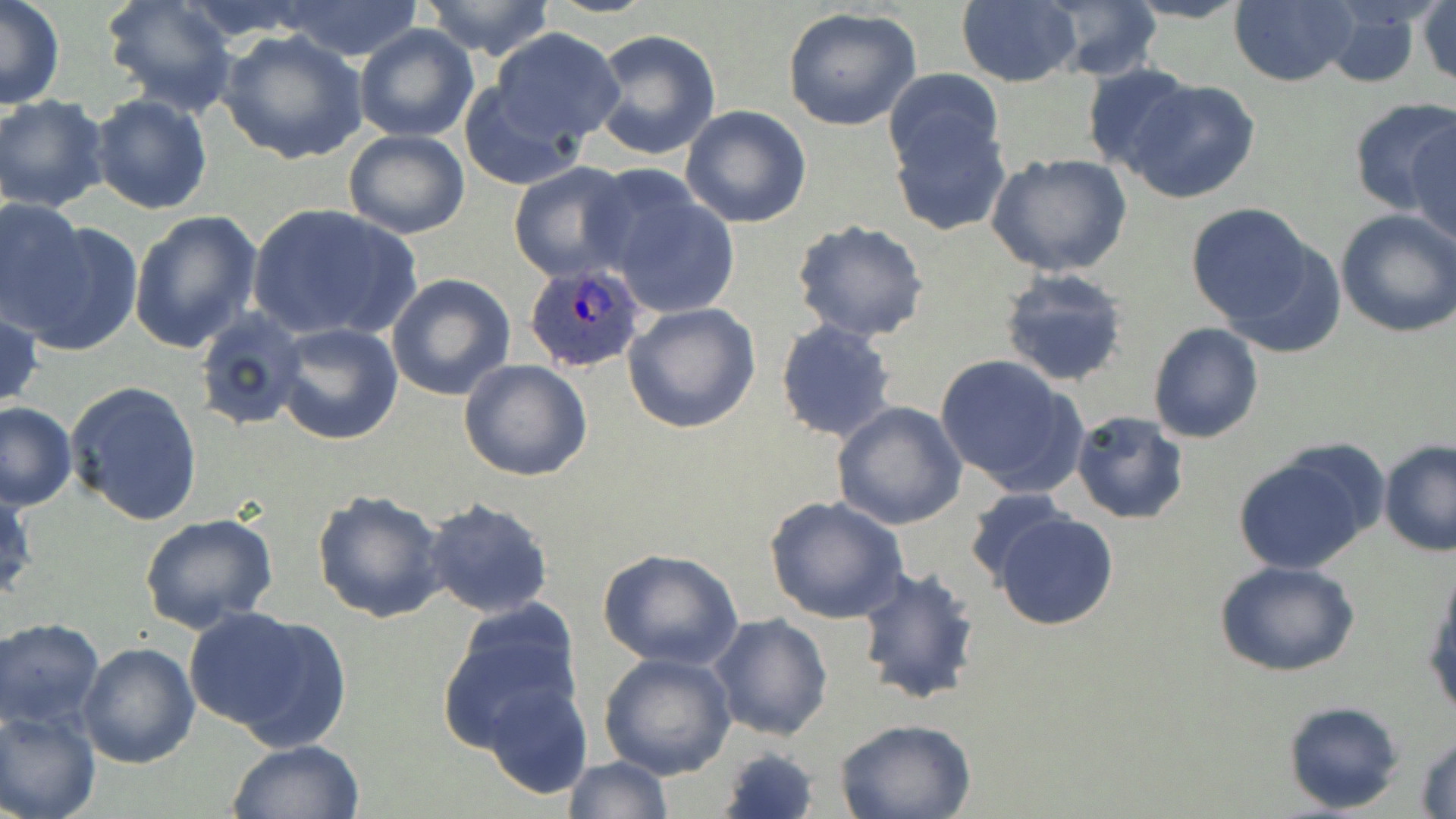
Summary:
  - Coordinate format: approximate bounding boxes as (x1,y1)-(x2,y2) corner pairs in pixels
  - Uninfected red blood cell locations: (0,0)-(66,110), (100,0)-(237,115), (419,0)-(558,60), (538,0)-(659,19), (956,0)-(1081,87), (1041,0)-(1162,81), (1119,0)-(1256,24), (1228,1)-(1357,87), (1418,1)-(1455,89), (277,3)-(426,61), (1320,5)-(1426,88), (782,6)-(923,133), (354,22)-(480,143), (489,28)-(627,147), (589,28)-(722,161), (216,29)-(369,165), (1081,63)-(1196,176), (883,67)-(1005,175), (1123,80)-(1262,204), (458,81)-(583,190), (89,92)-(214,215), (0,95)-(109,212), (1348,95)-(1454,219), (681,104)-(812,228), (889,110)-(1011,236), (1407,112)-(1455,247), (342,129)-(471,240), (987,153)-(1134,280), (508,161)-(639,281), (596,176)-(741,320), (1,196)-(89,322), (246,202)-(419,343), (1185,202)-(1321,335), (128,209)-(263,355), (1334,209)-(1456,338), (792,219)-(929,343), (11,220)-(143,356), (997,269)-(1130,388), (386,272)-(516,401), (622,301)-(763,435), (0,302)-(43,413), (193,305)-(306,431), (773,320)-(898,445), (274,322)-(404,444), (1147,322)-(1264,443), (933,354)-(1086,498), (459,359)-(593,481), (64,379)-(204,526), (0,401)-(77,511), (830,402)-(969,532), (1070,411)-(1189,524), (1378,438)-(1456,557), (1229,452)-(1374,575), (0,481)-(36,605), (964,488)-(1073,585), (312,489)-(448,623), (764,494)-(911,626), (423,498)-(555,618), (987,507)-(1120,632), (138,513)-(279,638), (597,548)-(744,670), (1217,562)-(1359,678), (855,565)-(985,708), (1423,565)-(1456,720), (439,601)-(585,750), (184,603)-(351,747), (709,613)-(834,742), (0,617)-(106,731), (77,643)-(200,769), (599,652)-(736,778), (480,679)-(594,800), (1281,700)-(1406,815), (0,708)-(101,819), (833,718)-(976,819), (1413,732)-(1456,817), (226,738)-(366,819), (716,745)-(822,819), (561,756)-(674,818)
  - Plasmodium ovale-infected red blood cell locations: (521,260)-(650,374)
  - Slide-level diagnosis: Plasmodium ovale
  - Field of view: single
  - Magnification: 1000x
  - Preparation: thin blood smear
  - Stain: May-Grünwald-Giemsa
  - Modality: light microscopy
  - Image size: 1456×819 pixels